Report the malaria status of this cell.
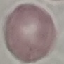

Uninfected.

Acquired by smartphone through the microscope eyepiece. Giemsa-stained preparation. Thin smear of blood. Automatically extracted cell patch, resized to 64 × 64 pixels.